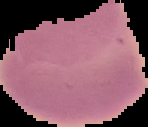 Result: negative for Plasmodium parasites. From a thin blood film. The area outside the segmented cell region is set to black. Image is 148×127 pixels.